Name the blood parasite species.
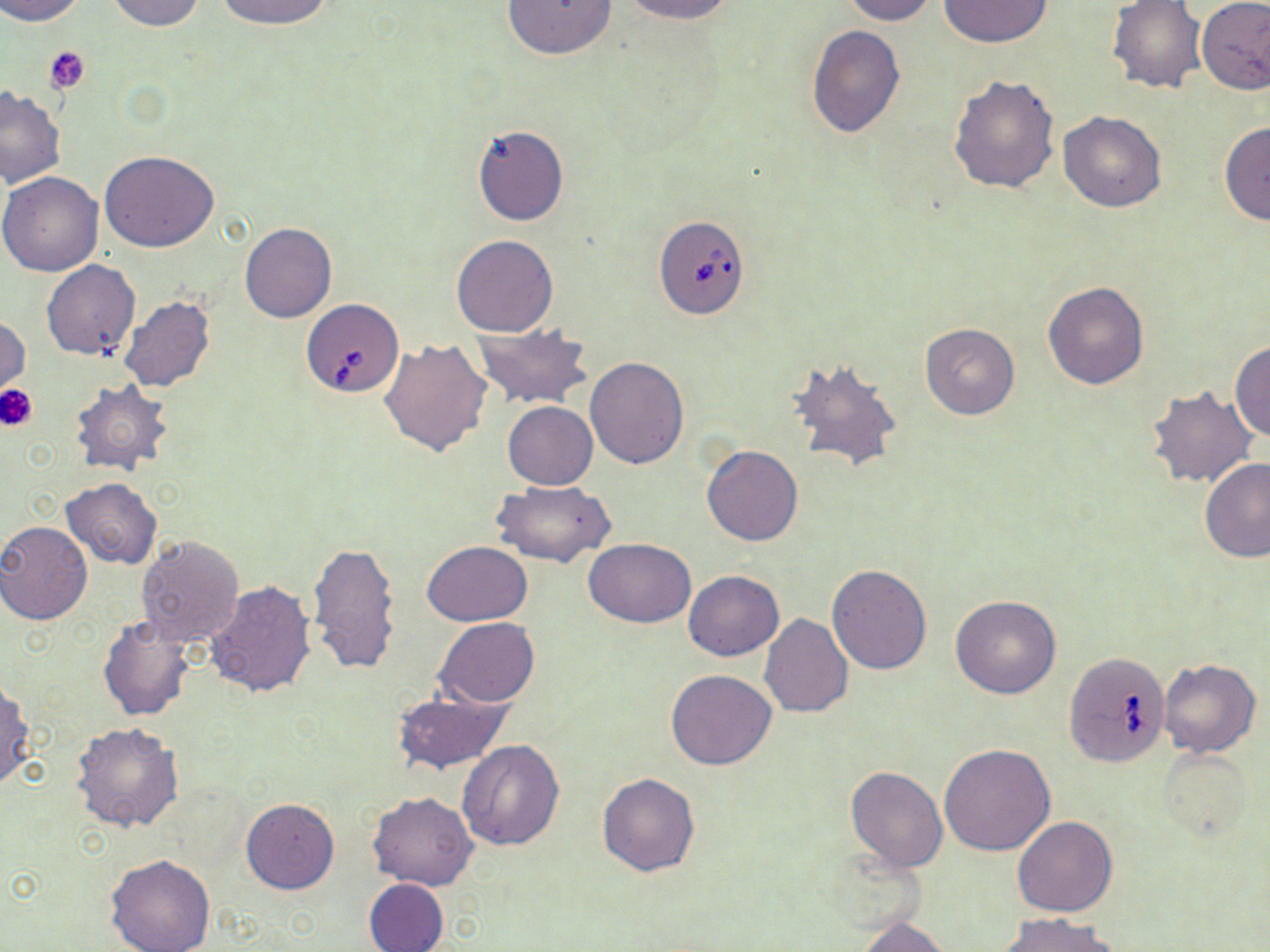
Babesia divergens.

platelet locations = approximate bounding boxes as named x1/y1/x2/y2 corners in pixels: (x1=44, y1=45, x2=92, y2=94), (x1=0, y1=384, x2=38, y2=430)
Babesia divergens-infected red blood cell locations = approximate bounding boxes as named x1/y1/x2/y2 corners in pixels: (x1=653, y1=213, x2=751, y2=320), (x1=305, y1=298, x2=405, y2=398), (x1=1063, y1=651, x2=1171, y2=768)
magnification = 1000x
stain = May-Grünwald-Giemsa
preparation = thin blood film
field of view = single
image size = 1270×952 pixels
uninfected red blood cell locations = approximate bounding boxes as named x1/y1/x2/y2 corners in pixels: (x1=0, y1=0, x2=86, y2=24), (x1=211, y1=0, x2=337, y2=28), (x1=503, y1=0, x2=618, y2=60), (x1=619, y1=0, x2=734, y2=24), (x1=841, y1=0, x2=937, y2=25), (x1=1106, y1=0, x2=1208, y2=95), (x1=1196, y1=0, x2=1270, y2=95), (x1=106, y1=1, x2=207, y2=31), (x1=937, y1=1, x2=1055, y2=47), (x1=806, y1=25, x2=905, y2=139), (x1=948, y1=73, x2=1061, y2=195), (x1=0, y1=86, x2=65, y2=187), (x1=1058, y1=111, x2=1168, y2=212), (x1=1219, y1=121, x2=1270, y2=225), (x1=470, y1=124, x2=569, y2=227), (x1=101, y1=151, x2=220, y2=252), (x1=0, y1=172, x2=104, y2=277), (x1=240, y1=222, x2=336, y2=323), (x1=450, y1=234, x2=558, y2=337), (x1=41, y1=260, x2=140, y2=361), (x1=1043, y1=281, x2=1151, y2=390), (x1=119, y1=297, x2=216, y2=392), (x1=1, y1=318, x2=30, y2=397), (x1=472, y1=323, x2=593, y2=410), (x1=920, y1=323, x2=1021, y2=420), (x1=380, y1=337, x2=493, y2=457), (x1=1230, y1=340, x2=1270, y2=441), (x1=584, y1=356, x2=689, y2=470), (x1=785, y1=357, x2=903, y2=474), (x1=69, y1=379, x2=174, y2=477), (x1=1144, y1=385, x2=1257, y2=489), (x1=503, y1=401, x2=598, y2=490), (x1=701, y1=445, x2=803, y2=546), (x1=1200, y1=456, x2=1269, y2=564), (x1=61, y1=477, x2=162, y2=569), (x1=492, y1=479, x2=615, y2=568), (x1=0, y1=521, x2=91, y2=624), (x1=134, y1=535, x2=244, y2=650), (x1=585, y1=539, x2=696, y2=627), (x1=307, y1=541, x2=403, y2=675), (x1=422, y1=541, x2=533, y2=625), (x1=826, y1=564, x2=932, y2=675), (x1=684, y1=570, x2=783, y2=660), (x1=205, y1=582, x2=318, y2=698), (x1=950, y1=595, x2=1061, y2=698), (x1=759, y1=614, x2=852, y2=718), (x1=97, y1=617, x2=194, y2=720), (x1=434, y1=618, x2=541, y2=706), (x1=1158, y1=659, x2=1261, y2=759), (x1=666, y1=669, x2=777, y2=769), (x1=0, y1=680, x2=34, y2=792), (x1=391, y1=690, x2=511, y2=774), (x1=71, y1=721, x2=184, y2=833), (x1=457, y1=739, x2=566, y2=851), (x1=939, y1=743, x2=1055, y2=856), (x1=1156, y1=747, x2=1255, y2=843), (x1=846, y1=766, x2=947, y2=871), (x1=597, y1=774, x2=699, y2=875), (x1=367, y1=791, x2=477, y2=890), (x1=241, y1=798, x2=339, y2=894), (x1=1012, y1=816, x2=1119, y2=917), (x1=104, y1=853, x2=215, y2=952), (x1=363, y1=878, x2=449, y2=952), (x1=1000, y1=913, x2=1119, y2=952), (x1=856, y1=916, x2=952, y2=952)
modality = light microscopy